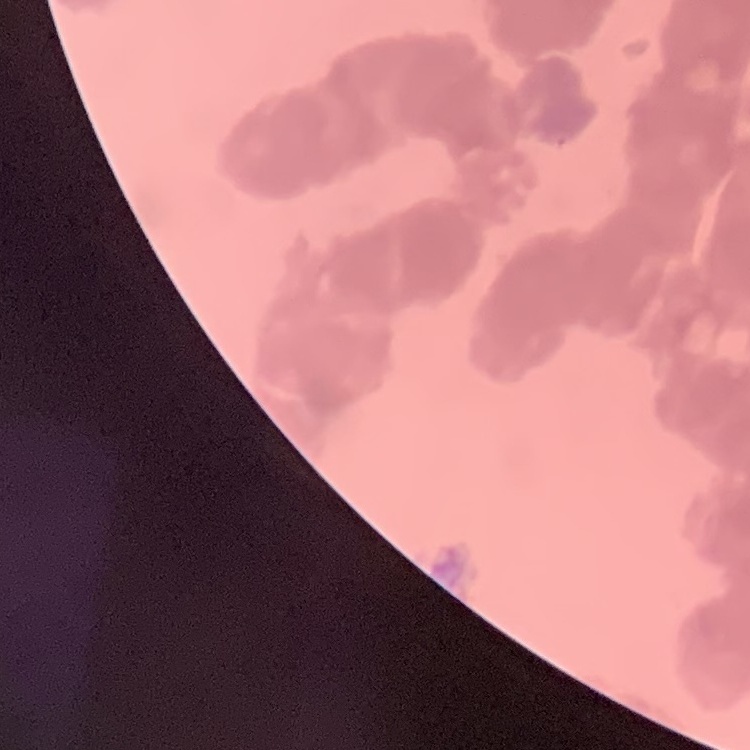

The red blood cells exhibit rouleaux formation. Thin peripheral smear. One tile cut from a larger photomicrograph. Field's or Giemsa stain.